Identify the parasite.
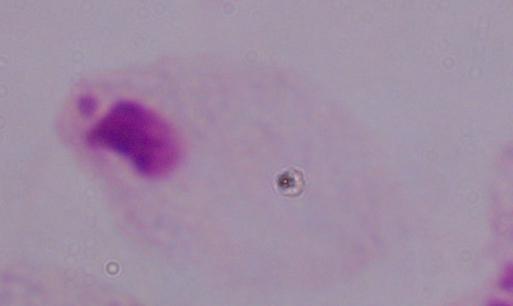

This is a trichomonad.

{
  "modality": "micrograph",
  "magnification": "1000x"
}